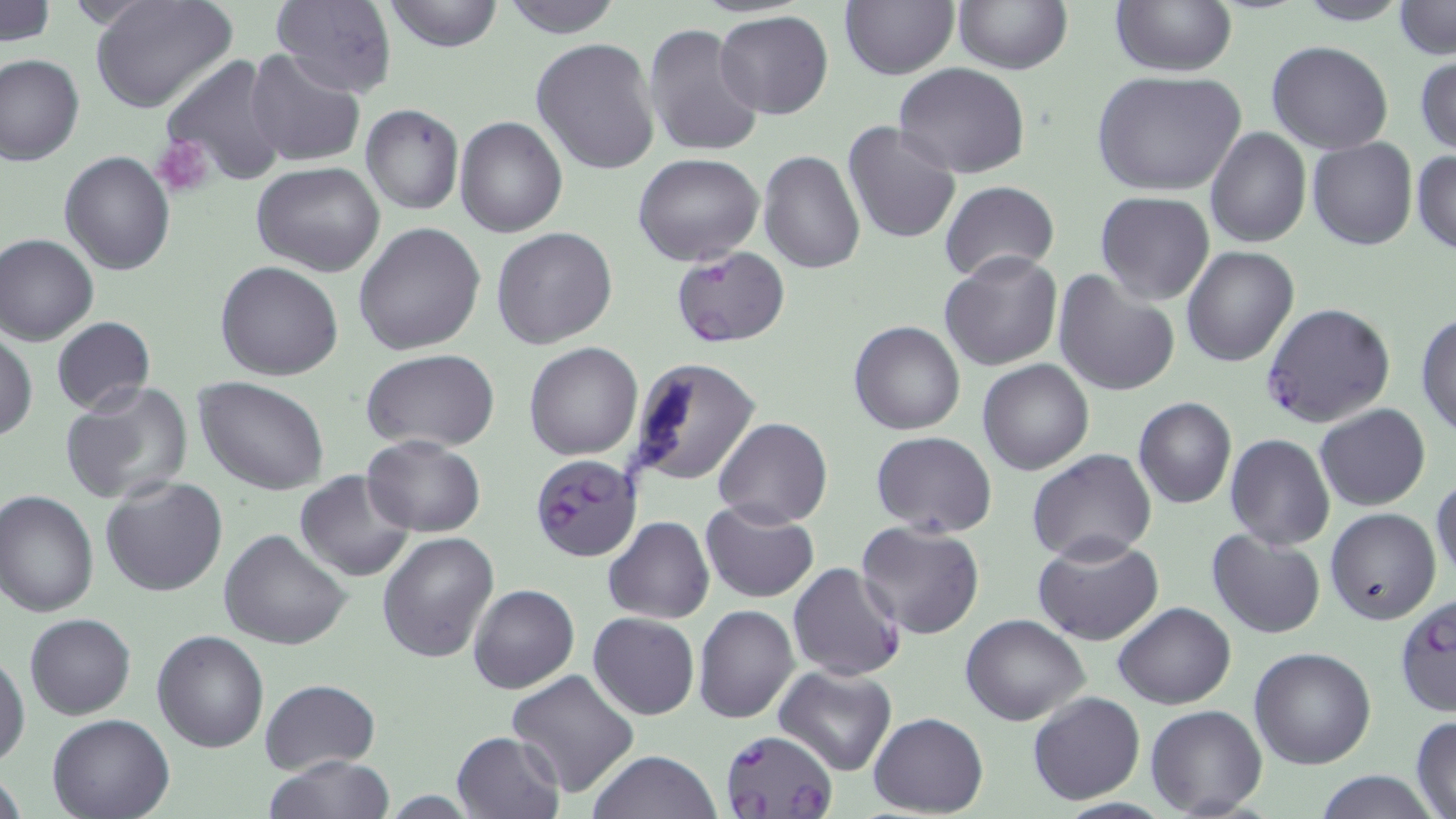

{
  "slide_level_diagnosis": "Plasmodium falciparum",
  "preparation": "thin blood smear",
  "plasmodium_falciparum_infected_red_blood_cell_locations": "approximate bounding boxes as (x1,y1)-(x2,y2) corner pairs in pixels: (671,248)-(788,348), (1263,302)-(1395,429), (530,453)-(640,562), (787,562)-(905,682), (720,729)-(839,819)",
  "uninfected_red_blood_cell_locations": "approximate bounding boxes as (x1,y1)-(x2,y2) corner pairs in pixels: (1,0)-(55,46), (88,0)-(238,115), (382,0)-(505,53), (499,0)-(624,38), (952,0)-(1072,74), (1109,0)-(1237,76), (1293,0)-(1411,26), (269,1)-(398,97), (1393,1)-(1454,60), (840,2)-(958,79), (715,11)-(834,120), (643,23)-(764,157), (533,37)-(661,178), (1266,39)-(1394,155), (245,48)-(366,168), (0,54)-(84,166), (1415,54)-(1456,155), (160,57)-(292,189), (894,62)-(1030,179), (1090,70)-(1246,196), (360,104)-(464,215), (456,115)-(568,237), (841,121)-(961,245), (1206,127)-(1311,248), (1307,137)-(1418,251), (1412,149)-(1456,256), (59,151)-(175,275), (758,151)-(864,274), (633,153)-(764,265), (251,161)-(386,277), (940,180)-(1059,285), (1096,192)-(1215,306), (355,221)-(486,356), (491,228)-(617,348), (1,233)-(98,345), (1182,245)-(1298,366), (939,251)-(1064,371), (215,261)-(344,381), (1051,270)-(1180,398), (1415,311)-(1456,440), (50,317)-(155,415), (849,320)-(966,435), (1,332)-(37,442), (524,343)-(642,460), (359,350)-(499,453), (625,357)-(761,488), (977,359)-(1095,474), (195,378)-(331,495), (60,381)-(193,506), (1133,396)-(1238,508), (1315,404)-(1430,510), (714,417)-(833,528), (870,432)-(997,537), (1225,434)-(1335,551), (361,435)-(484,536), (1027,450)-(1156,566), (295,470)-(414,581), (1432,473)-(1455,584), (101,476)-(228,598), (0,491)-(99,616), (700,502)-(818,601), (1326,507)-(1441,626), (604,516)-(714,623), (857,520)-(987,639), (219,527)-(351,650), (1207,528)-(1326,640), (377,530)-(499,664), (1033,536)-(1165,645), (467,583)-(579,693), (1393,592)-(1456,719), (1113,602)-(1235,709), (694,604)-(798,723), (32,609)-(148,819), (588,612)-(699,719), (25,613)-(136,720), (960,614)-(1090,726), (152,629)-(268,753), (1249,646)-(1377,769), (1,652)-(30,767), (772,666)-(897,776), (505,668)-(641,798), (261,678)-(380,773), (1027,692)-(1145,805), (1146,704)-(1266,817), (868,713)-(988,817), (48,714)-(175,819), (1410,715)-(1455,818), (451,731)-(564,819), (587,751)-(722,819), (264,756)-(396,819), (1312,769)-(1437,819)",
  "magnification": "1000x",
  "modality": "optical microscopy",
  "platelet_locations": "approximate bounding boxes as (x1,y1)-(x2,y2) corner pairs in pixels: (153,137)-(216,199)",
  "stain": "May-Grünwald-Giemsa",
  "field_of_view": "single",
  "image_size": "1456×819 pixels"
}